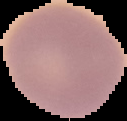
Summary:
  - Preparation: thin blood smear
  - Image type: segmented cell region with the area outside set to black
  - Image size: 127×121 pixels
  - Result: no malaria parasites detected